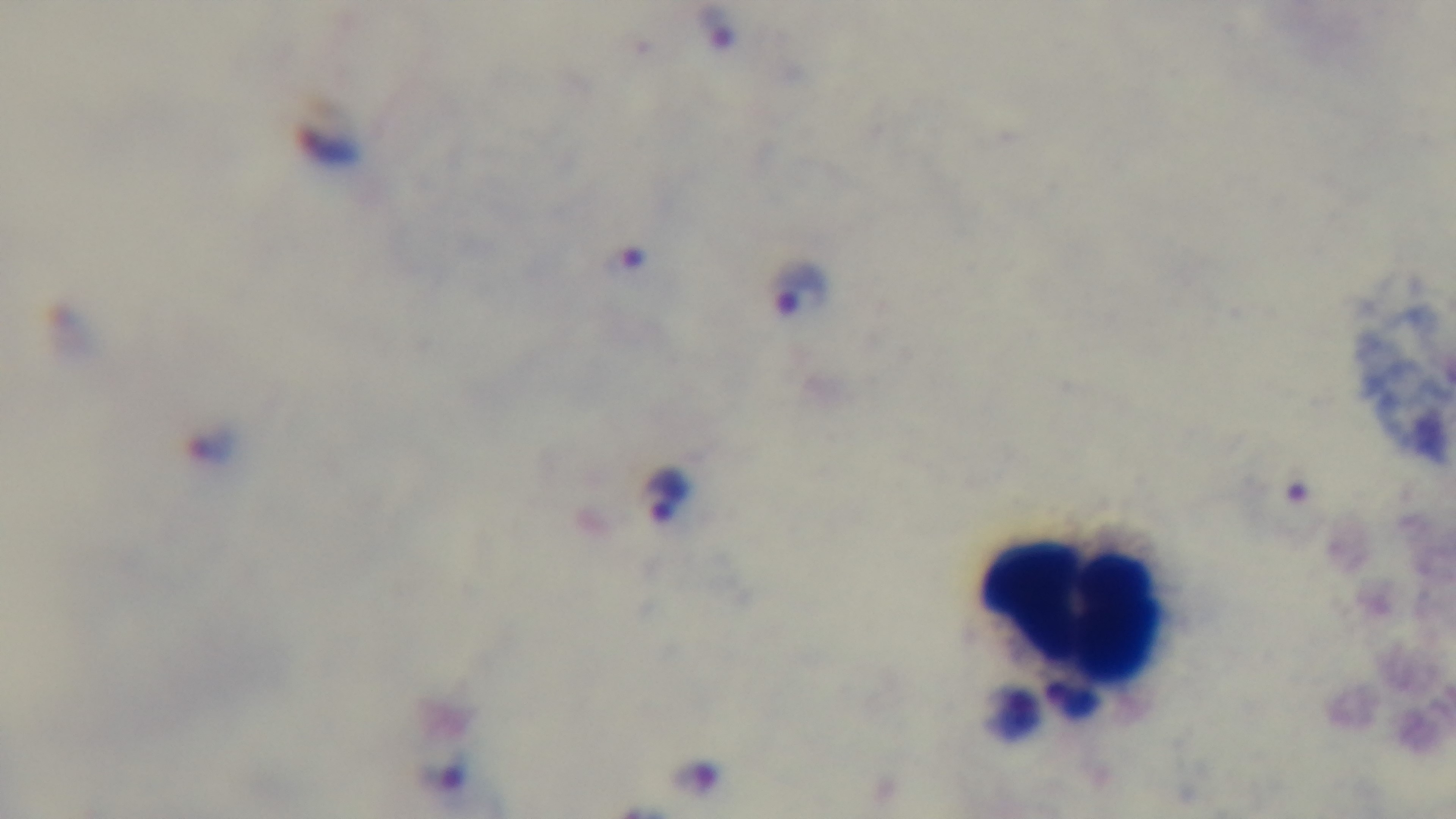

Summary:
  - Objective: 100x oil immersion
  - Malaria status: positive
  - Capture: mounted 4K digital camera
  - Stain: Giemsa
  - Modality: light microscopy
  - Preparation: thick smear
  - Field of view: one from the slide